State which parasite is depicted.
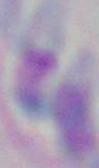
Toxoplasma gondii.

{
  "modality": "photomicrograph",
  "magnification": "1000x"
}